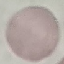

Malaria status: uninfected. Thin blood film. Giemsa stain. Automatically extracted cell patch, resized to 64 × 64 pixels. Photographed with a smartphone camera at the microscope eyepiece.